Classify this cell by malaria status.
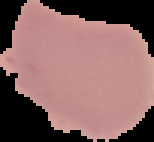

It is uninfected.

{
  "image_size": "154×142 pixels",
  "preparation": "thin blood film",
  "image_type": "segmented cell region on a black background"
}